State which parasite is depicted.
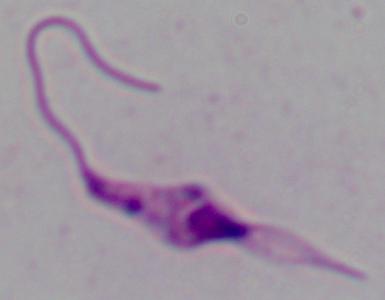
This is Leishmania.

Summary:
  - Modality: micrograph
  - Magnification: 1000x